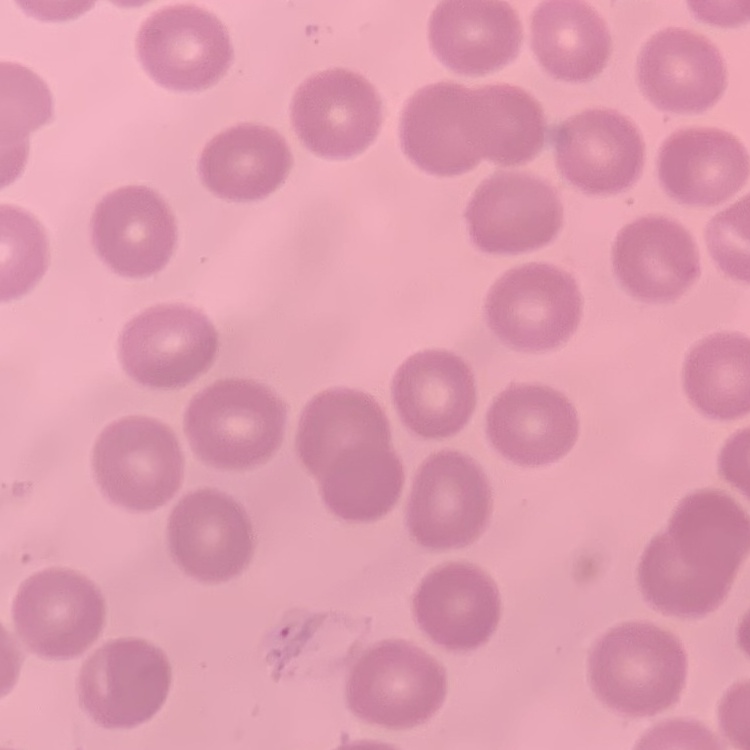
The erythrocytes show no rouleaux formation. One tile cut from a larger photomicrograph. Field's or Giemsa stain. Thin blood smear.